Assess this cell for malaria.
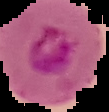
Parasitized.

image size = 109×112 pixels
image type = segmented cell region with the area outside set to black
preparation = thin blood film